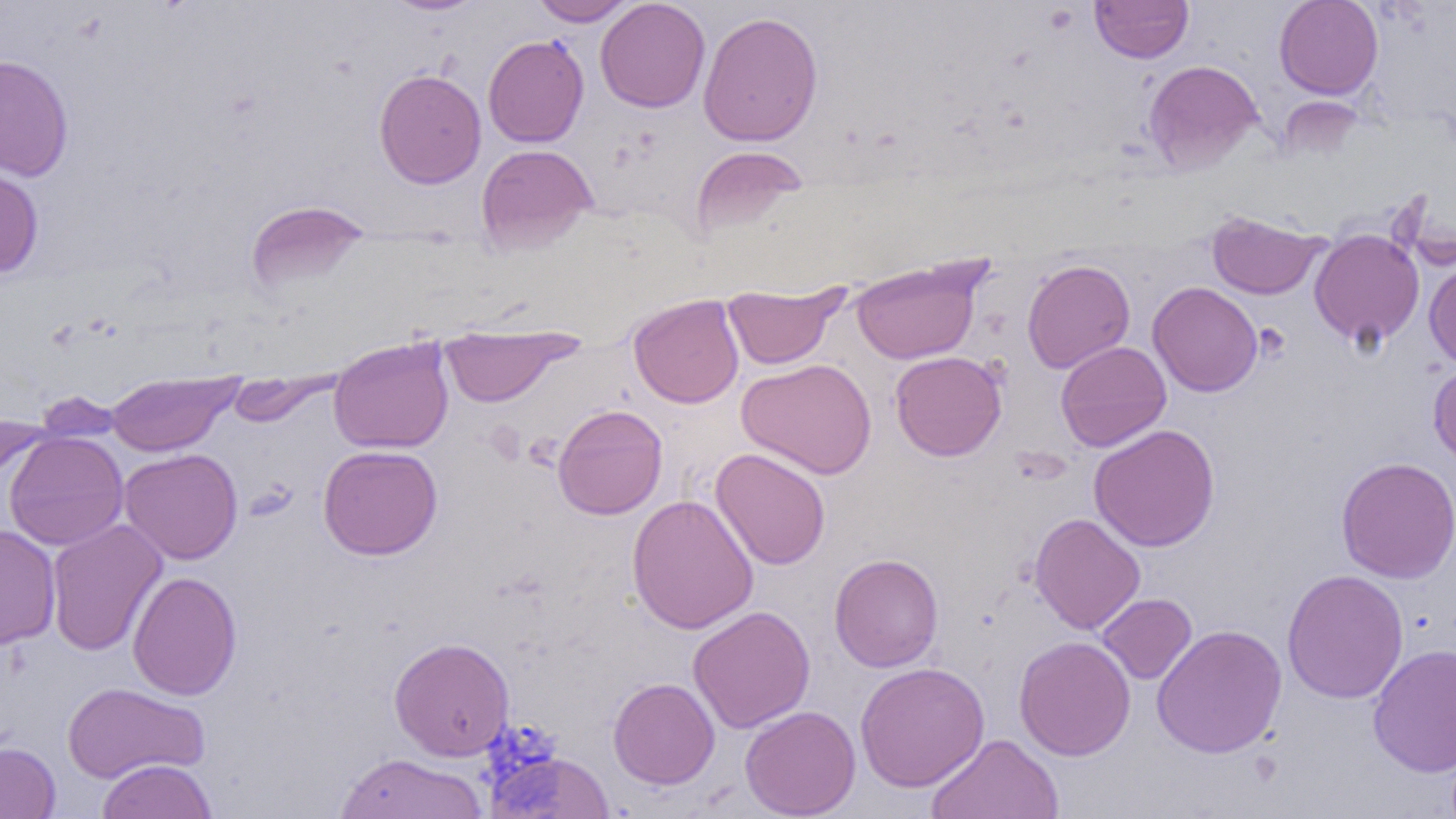
slide-level diagnosis = negative for blood parasites
uninfected red blood cell locations = approximate bounding boxes as (x1, y1, x2, y2) in pixels: (381, 0, 491, 16), (529, 0, 636, 26), (595, 0, 710, 113), (1090, 0, 1193, 63), (1273, 0, 1383, 100), (697, 11, 823, 147), (483, 34, 589, 148), (0, 53, 74, 181), (1143, 59, 1263, 173), (373, 68, 487, 188), (476, 143, 598, 253), (689, 145, 810, 237), (0, 164, 44, 278), (245, 200, 371, 294), (1206, 210, 1329, 300), (1309, 228, 1425, 349), (850, 256, 988, 365), (1022, 259, 1135, 374), (1424, 260, 1456, 370), (1147, 281, 1263, 397), (722, 282, 847, 370), (628, 294, 744, 408), (439, 326, 580, 408), (328, 336, 454, 453), (1055, 341, 1172, 452), (889, 351, 1007, 461), (736, 358, 877, 479), (1428, 361, 1456, 469), (105, 371, 242, 456), (226, 372, 339, 427), (552, 404, 668, 519), (0, 411, 51, 497), (1088, 424, 1220, 552), (3, 431, 129, 551), (318, 444, 443, 560), (119, 448, 243, 565), (710, 448, 831, 570), (1335, 456, 1456, 583), (627, 494, 759, 635), (1029, 513, 1145, 635), (46, 519, 167, 656), (0, 524, 61, 650), (828, 553, 944, 672), (1282, 568, 1409, 704), (127, 571, 242, 700), (1096, 593, 1197, 685), (688, 605, 816, 733), (1151, 623, 1287, 759), (1014, 635, 1136, 761), (388, 637, 515, 761), (1368, 643, 1456, 777), (854, 661, 990, 792), (608, 677, 720, 790), (61, 682, 210, 783), (740, 704, 861, 819), (927, 733, 1064, 819), (0, 741, 61, 818), (485, 750, 615, 818), (335, 752, 489, 818), (95, 758, 218, 819)
field of view = one of a larger specimen
modality = optical microscopy
image size = 1456×819 pixels
preparation = thin blood film
magnification = 1000x